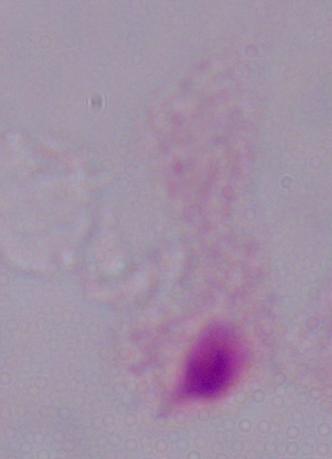

Summary:
  - Magnification: 1000x
  - Modality: micrograph
  - Identification: trichomonad